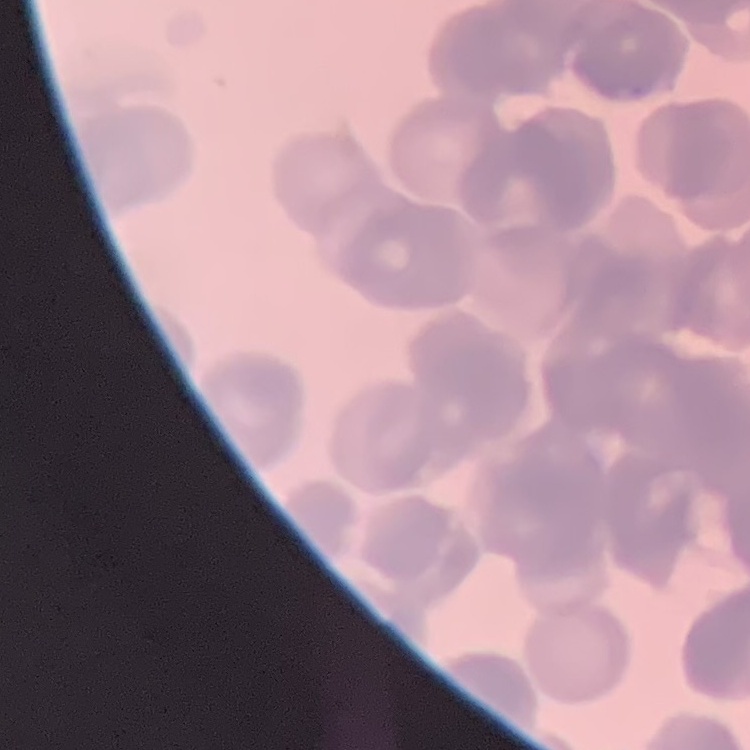

The red blood cells show rouleaux formation. Stained with either Field's or Giemsa. One tile cut from a larger photomicrograph. Thin peripheral smear.